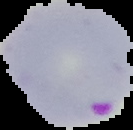

Summary:
  - Image size: 133×130 pixels
  - Image type: cell region segmented out of the field of view; surrounding area masked to black
  - Preparation: thin blood film
  - Malaria status: parasitized